Outline each Plasmodium falciparum-infected red blood cell.
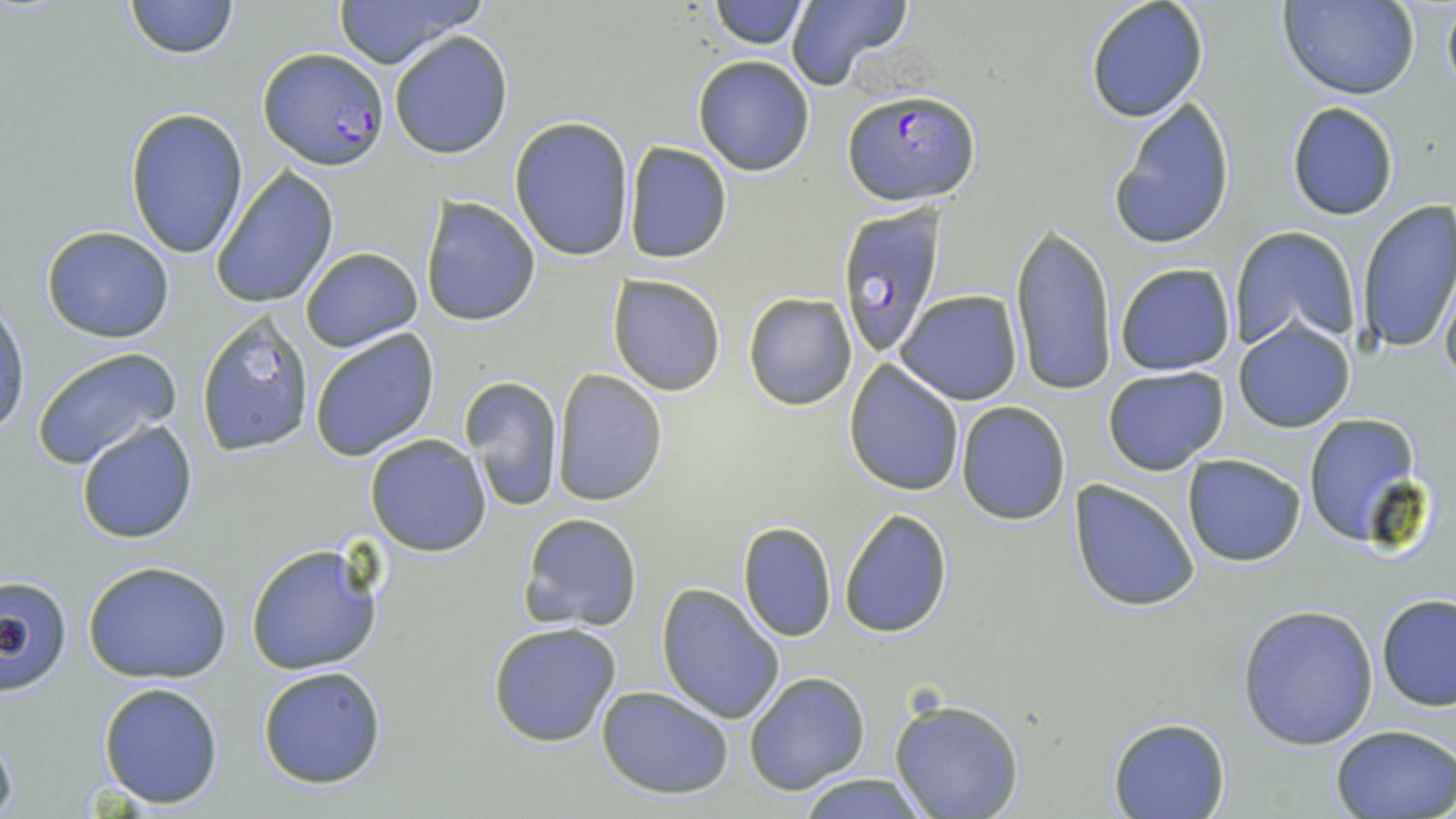

Approximate bounding boxes as (x1,y1)-(x2,y2) corner pairs in pixels.
Plasmodium falciparum-infected red blood cells: (254,49)-(387,172), (842,91)-(980,206), (836,204)-(947,360).

slide-level diagnosis = Plasmodium falciparum
uninfected red blood cell locations = approximate bounding boxes as (x1,y1)-(x2,y2) corner pairs in pixels: (124,0)-(239,59), (331,0)-(484,69), (711,0)-(809,49), (783,0)-(912,93), (1085,0)-(1210,124), (1277,0)-(1420,101), (1441,0)-(1456,101), (389,31)-(513,160), (693,56)-(816,176), (1107,95)-(1236,251), (1285,100)-(1401,221), (126,107)-(248,260), (509,116)-(634,263), (625,142)-(732,264), (211,167)-(340,308), (421,196)-(540,327), (1356,198)-(1456,356), (1010,221)-(1117,398), (40,225)-(174,343), (1229,226)-(1359,354), (299,246)-(424,351), (1113,264)-(1236,376), (608,275)-(726,395), (1439,275)-(1456,388), (895,290)-(1022,404), (742,292)-(857,411), (1,298)-(30,437), (195,311)-(316,458), (1235,319)-(1355,432), (309,331)-(440,462), (30,346)-(180,470), (844,360)-(965,495), (1101,367)-(1230,476), (552,370)-(667,506), (460,375)-(564,510), (955,401)-(1071,524), (1303,412)-(1420,544), (77,419)-(198,544), (365,434)-(492,556), (1183,454)-(1306,567), (1070,479)-(1201,612), (839,508)-(953,639), (517,512)-(643,633), (736,521)-(838,642), (244,541)-(385,677), (82,560)-(232,683), (2,576)-(71,690), (657,583)-(786,725), (1375,594)-(1456,711), (1238,603)-(1378,749), (486,622)-(624,749), (257,665)-(389,789), (743,672)-(870,795), (97,681)-(223,809), (596,685)-(736,800), (886,696)-(1026,819), (1107,716)-(1233,819), (1331,724)-(1456,818), (0,730)-(19,818), (797,773)-(927,818)
image size = 1456×819 pixels
preparation = thin blood smear
stain = May-Grünwald-Giemsa
magnification = 1000x
field of view = one of a larger specimen
modality = light microscopy